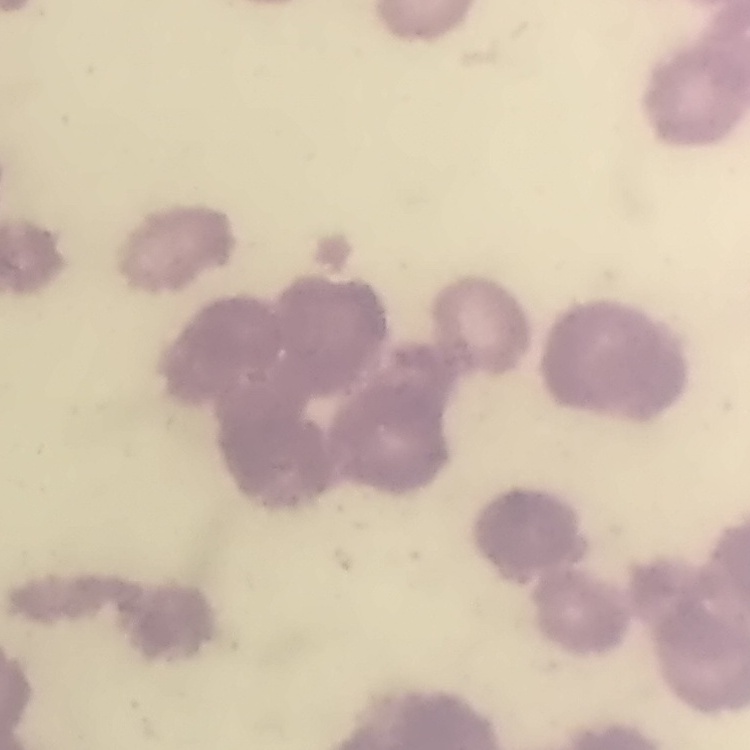

red blood cell morphology = rouleaux formation
stain = Field's or Giemsa
preparation = thin peripheral smear
image type = one tile cut from a larger photomicrograph